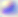
Summary:
  - Identification: Toxoplasma gondii
  - Magnification: 400x
  - Modality: micrograph